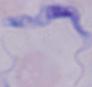
Summary:
  - Modality: micrograph
  - Identification: trypanosome
  - Magnification: 1000x